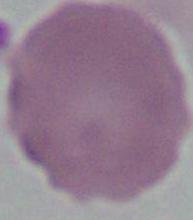

identification = erythrocyte
magnification = 1000x
modality = micrograph